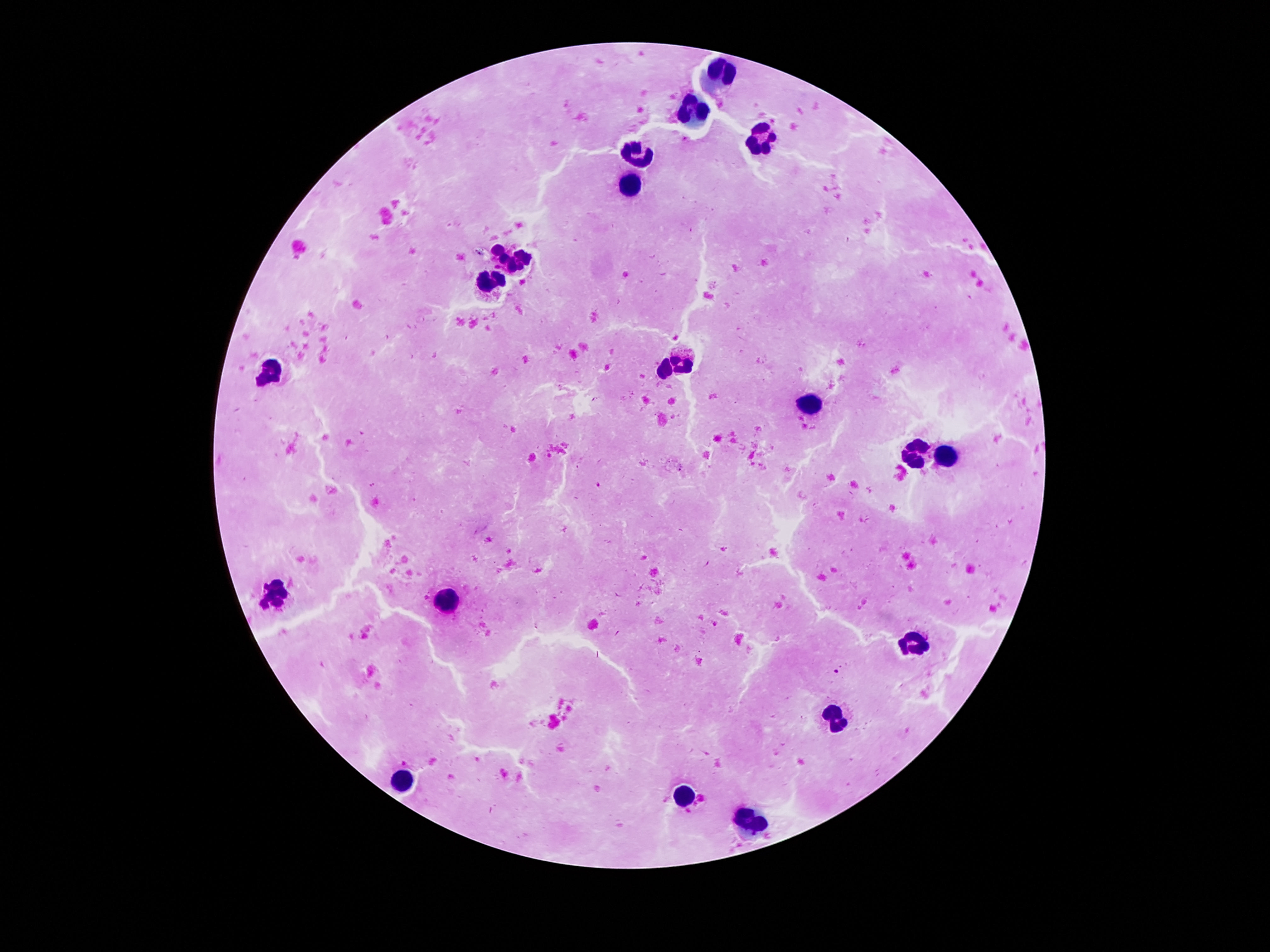
magnification = 100x
image size = 1270×952 pixels
leukocyte locations = approximate centers as [x, y] in pixels: [721, 69], [696, 110], [763, 140], [640, 151], [632, 183], [496, 248], [525, 256], [511, 267], [489, 284], [684, 356], [665, 368], [273, 374], [813, 405], [917, 454], [948, 456], [279, 594], [447, 599], [915, 646], [837, 716], [407, 780], [685, 796], [749, 825]
capture = smartphone camera through the microscope eyepiece
patient malaria status = negative
field of view = single
preparation = thick blood smear
stain = Giemsa